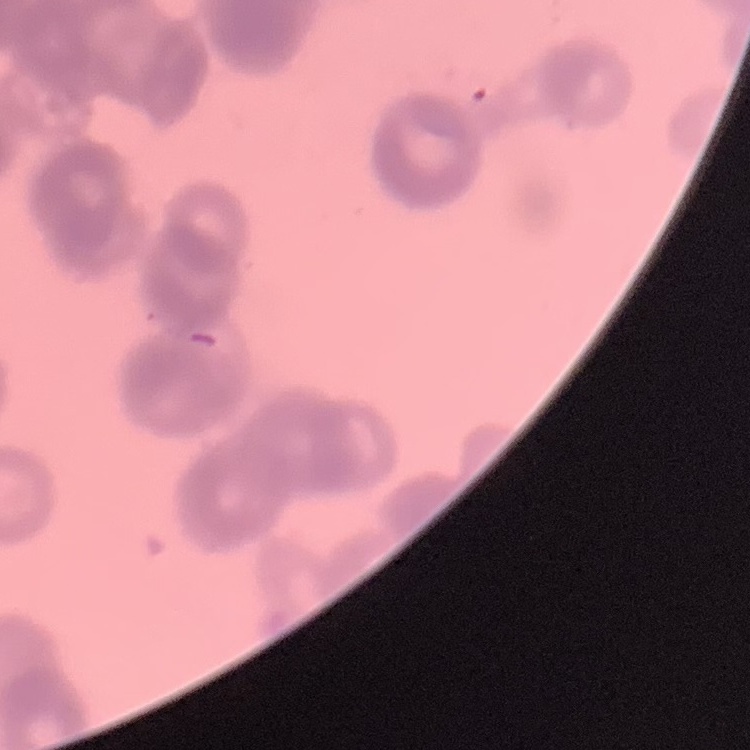 The red blood cells exhibit rouleaux formation. Square crop of a larger photomicrograph. Thin blood smear. Stained with either Field's or Giemsa.